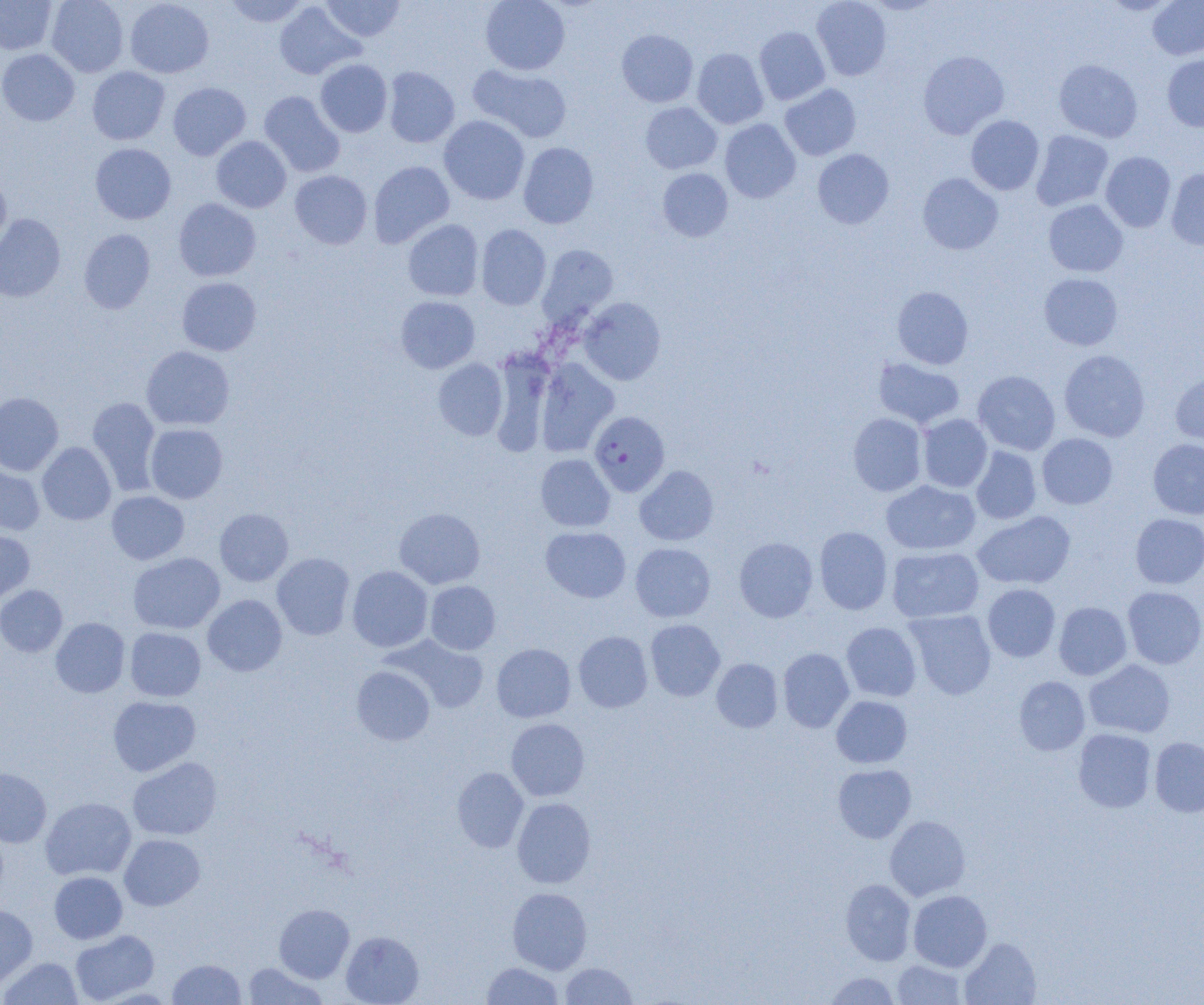
Approximate bounding boxes as (x1,y1)-(x2,y2) corner pairs in pixels. Plasmodium falciparum-infected red blood cell locations: (589,411)-(670,496). Uninfected red blood cell locations: (0,0)-(57,54), (46,0)-(128,77), (124,0)-(214,78), (224,0)-(310,27), (321,0)-(405,42), (480,0)-(570,75), (811,0)-(892,81), (1147,0)-(1204,60), (274,1)-(364,80), (754,26)-(830,105), (616,29)-(698,107), (0,48)-(80,126), (692,48)-(769,129), (918,50)-(1009,139), (1162,53)-(1204,131), (315,59)-(392,137), (1054,59)-(1143,143), (468,64)-(572,142), (87,66)-(170,145), (383,67)-(460,148), (168,82)-(251,160), (780,84)-(861,160), (259,91)-(344,177), (640,102)-(722,174), (966,115)-(1044,195), (439,116)-(530,205), (720,119)-(801,203), (1031,130)-(1113,211), (211,136)-(291,213), (518,142)-(598,228), (90,143)-(176,224), (812,148)-(894,229), (1100,151)-(1176,232), (368,161)-(454,248), (657,168)-(733,242), (1166,168)-(1204,250), (290,170)-(372,249), (918,173)-(1003,254), (0,174)-(11,250), (173,198)-(261,282), (1043,199)-(1128,277), (0,213)-(66,302), (403,220)-(484,301), (476,224)-(551,310), (79,229)-(155,314), (538,244)-(618,325), (1039,273)-(1123,350), (176,277)-(262,356), (891,286)-(974,369), (395,296)-(480,373), (578,297)-(666,385), (493,345)-(550,462), (141,346)-(234,430), (1058,350)-(1150,442), (433,358)-(508,440), (873,358)-(965,429), (535,359)-(619,456), (973,370)-(1060,455), (1170,370)-(1204,450), (0,392)-(63,476), (87,397)-(161,495), (848,412)-(927,496), (918,414)-(992,492), (145,423)-(228,503), (1037,433)-(1118,509), (1147,438)-(1204,519), (37,442)-(116,525), (971,446)-(1041,524), (536,454)-(615,531), (0,464)-(45,535), (635,466)-(718,546), (881,480)-(980,555), (107,491)-(189,564), (214,508)-(293,586), (394,508)-(485,589), (973,510)-(1076,590), (1130,513)-(1204,589), (540,526)-(631,603), (814,526)-(893,614), (0,530)-(35,603), (734,537)-(818,622), (630,543)-(715,622), (887,546)-(984,623), (128,552)-(225,633), (272,553)-(355,640), (347,565)-(433,652), (425,581)-(500,655), (982,583)-(1060,662), (0,585)-(67,657), (1122,586)-(1204,669), (202,595)-(287,676), (1054,602)-(1132,680), (905,609)-(996,700), (51,617)-(130,697), (645,619)-(725,701), (841,622)-(922,702), (125,627)-(206,701), (573,631)-(653,712), (385,635)-(488,714), (491,643)-(576,722), (777,648)-(855,732), (711,658)-(783,732), (1083,659)-(1175,738), (352,665)-(435,745), (1014,676)-(1090,755), (831,695)-(912,768), (108,696)-(200,776), (506,718)-(590,801), (1073,728)-(1156,813), (1149,737)-(1204,817), (128,757)-(222,840), (833,764)-(916,843), (0,767)-(51,847), (452,767)-(529,852), (40,797)-(136,881), (512,797)-(596,888), (884,815)-(970,901), (119,834)-(205,911), (49,871)-(127,943), (840,879)-(916,965), (507,887)-(592,974), (908,890)-(992,972), (0,904)-(38,990), (274,904)-(354,983), (70,929)-(159,1004), (341,931)-(423,1005), (959,937)-(1041,1005), (1,957)-(83,1004), (168,958)-(246,1004), (892,959)-(966,1005), (243,962)-(326,1004), (481,962)-(563,1004), (560,962)-(637,1004), (824,971)-(901,1004). Slide-level diagnosis: Plasmodium falciparum. Thin blood film. Single field of view. Optical microscopy. 1000x magnification. Image is 1204×1005 pixels.